Locate every blood parasite and identify its species.
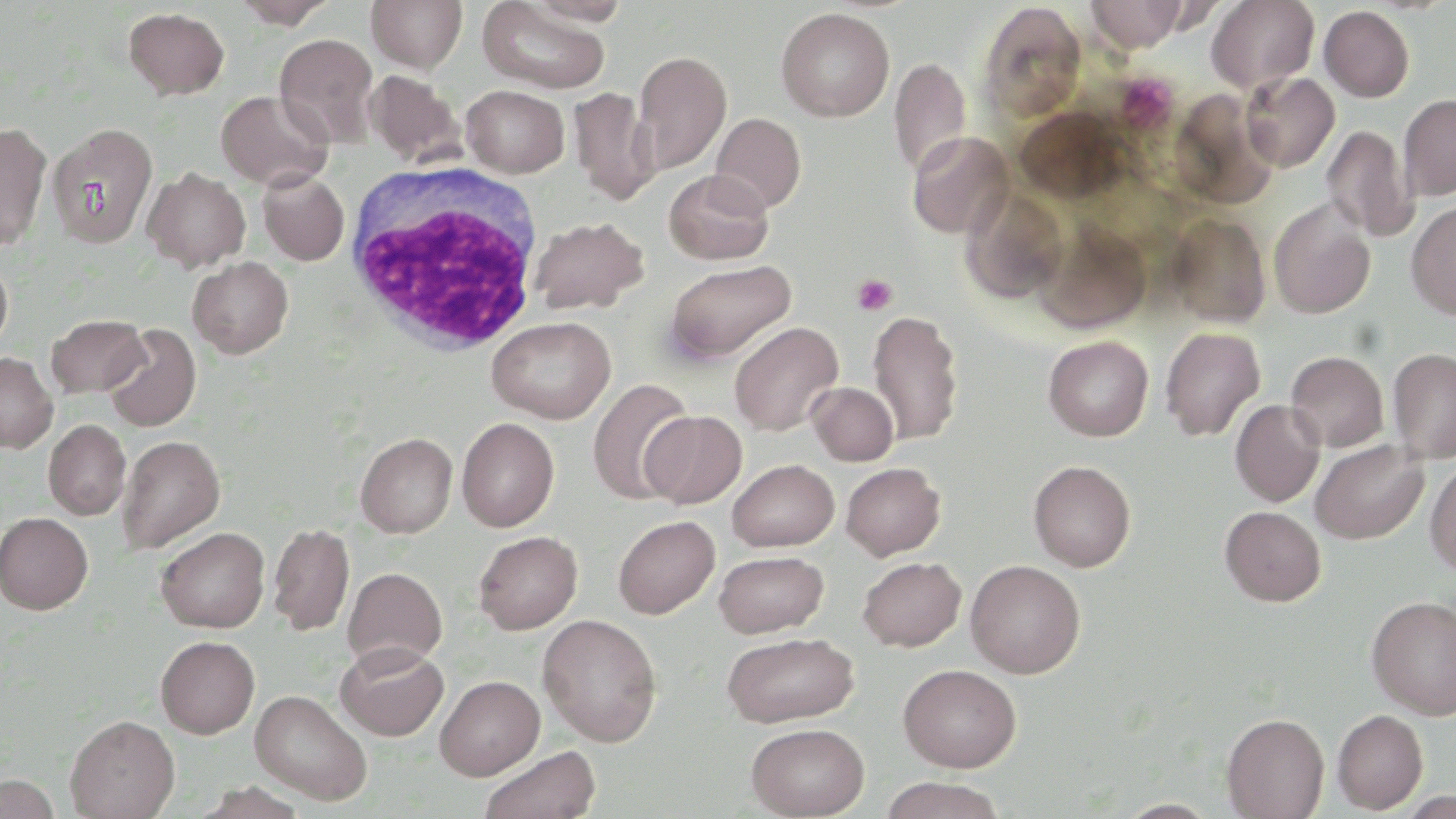

No blood parasites observed.

Approximate bounding boxes as (x1, y1, x2, y2) in pixels. Uninfected red blood cell locations: (230, 0, 338, 28), (366, 0, 468, 72), (1087, 0, 1185, 51), (1206, 0, 1320, 92), (477, 2, 611, 93), (977, 2, 1087, 122), (1320, 5, 1415, 102), (776, 7, 895, 121), (124, 8, 230, 99), (274, 33, 379, 147), (632, 50, 732, 174), (890, 57, 971, 178), (365, 71, 463, 166), (1241, 72, 1339, 172), (461, 85, 570, 177), (569, 87, 658, 204), (215, 90, 333, 191), (1399, 94, 1456, 200), (710, 112, 806, 214), (0, 122, 52, 252), (47, 123, 158, 247), (1322, 125, 1418, 245), (906, 131, 1014, 238), (143, 167, 251, 271), (663, 169, 775, 265), (257, 171, 349, 265), (1268, 199, 1376, 318), (1406, 201, 1456, 320), (1166, 214, 1271, 327), (530, 216, 647, 314), (1034, 221, 1152, 333), (0, 255, 13, 355), (188, 256, 293, 358), (664, 259, 796, 364), (868, 309, 964, 444), (46, 314, 150, 398), (487, 315, 616, 423), (729, 321, 844, 436), (102, 323, 201, 432), (1160, 327, 1265, 440), (1043, 335, 1154, 441), (1388, 346, 1456, 462), (1286, 351, 1388, 451), (0, 352, 58, 452), (587, 378, 695, 505), (807, 381, 899, 466), (1230, 400, 1325, 507), (641, 410, 747, 509), (456, 417, 559, 532), (43, 420, 131, 520), (355, 432, 457, 538), (117, 435, 225, 553), (1310, 440, 1428, 544), (727, 459, 839, 551), (1425, 459, 1456, 577), (1028, 460, 1136, 572), (841, 462, 945, 560), (1219, 505, 1325, 606), (0, 512, 93, 614), (613, 515, 720, 619), (268, 523, 355, 636), (156, 526, 269, 633), (473, 531, 582, 634), (714, 550, 829, 637), (857, 556, 966, 650), (965, 559, 1086, 678), (343, 567, 447, 669), (1366, 595, 1456, 719), (537, 614, 662, 747), (722, 631, 860, 727), (156, 635, 259, 738), (335, 642, 449, 740), (898, 663, 1022, 772), (434, 675, 545, 780), (250, 690, 373, 805), (1332, 709, 1428, 813), (1222, 712, 1329, 819), (65, 714, 179, 819), (746, 722, 870, 818), (479, 744, 602, 819), (0, 773, 61, 819), (878, 776, 1008, 819), (1114, 798, 1222, 818). White blood cell locations: (344, 165, 547, 357). Platelet locations: (851, 274, 898, 316). Slide-level diagnosis: negative for blood parasites. May-Grünwald-Giemsa-stained preparation. 1000x magnification. Single field of view. Optical microscopy. Thin blood film. Image is 1456×819 pixels.